Report the malaria status.
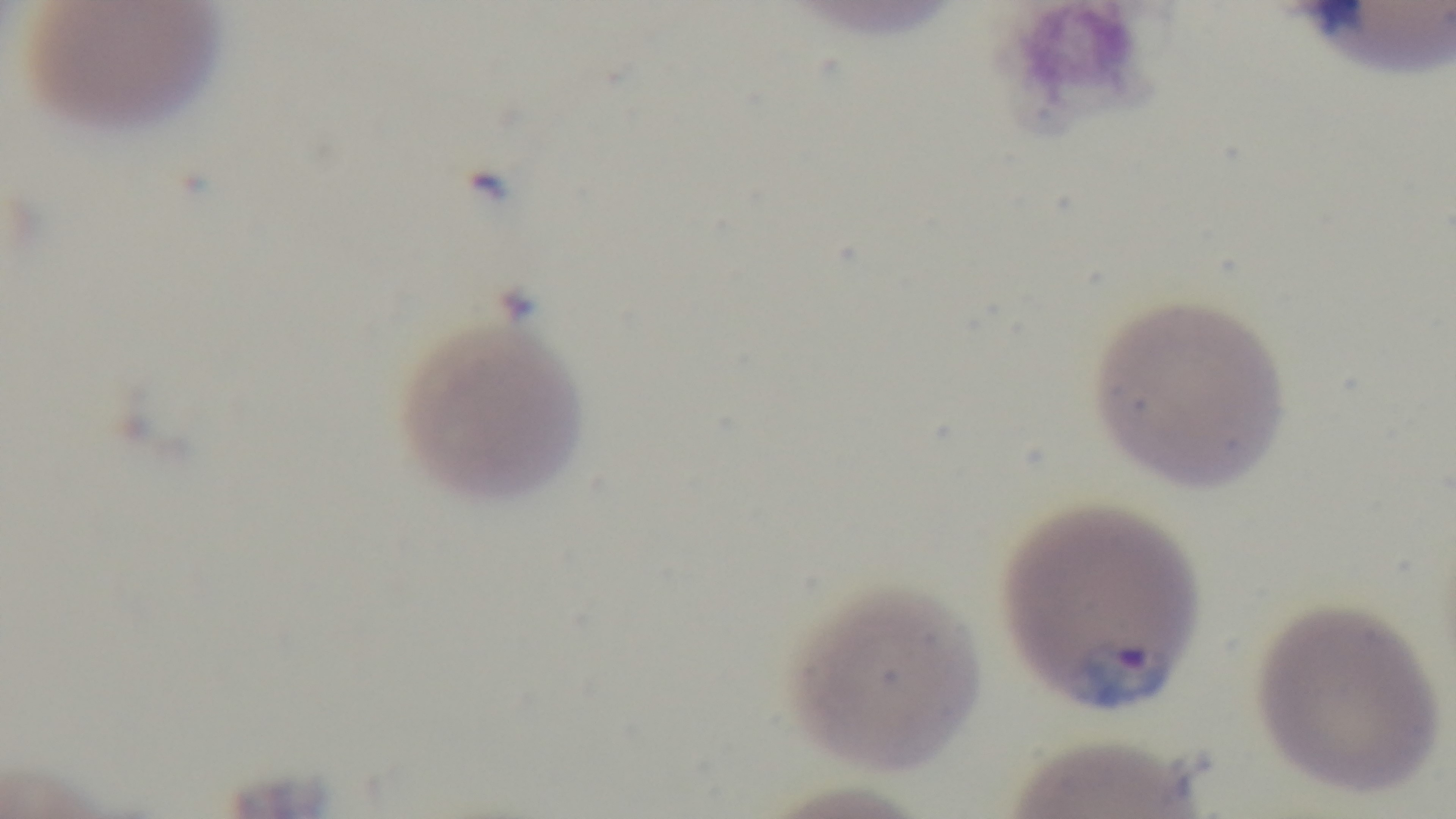
Infected.

Summary:
  - Modality: light microscopy
  - Field of view: single
  - Stain: Giemsa
  - Capture: mounted 4K digital camera
  - Objective: 100x oil immersion
  - Preparation: thin smear